Locate every Plasmodium ovale-infected red blood cell.
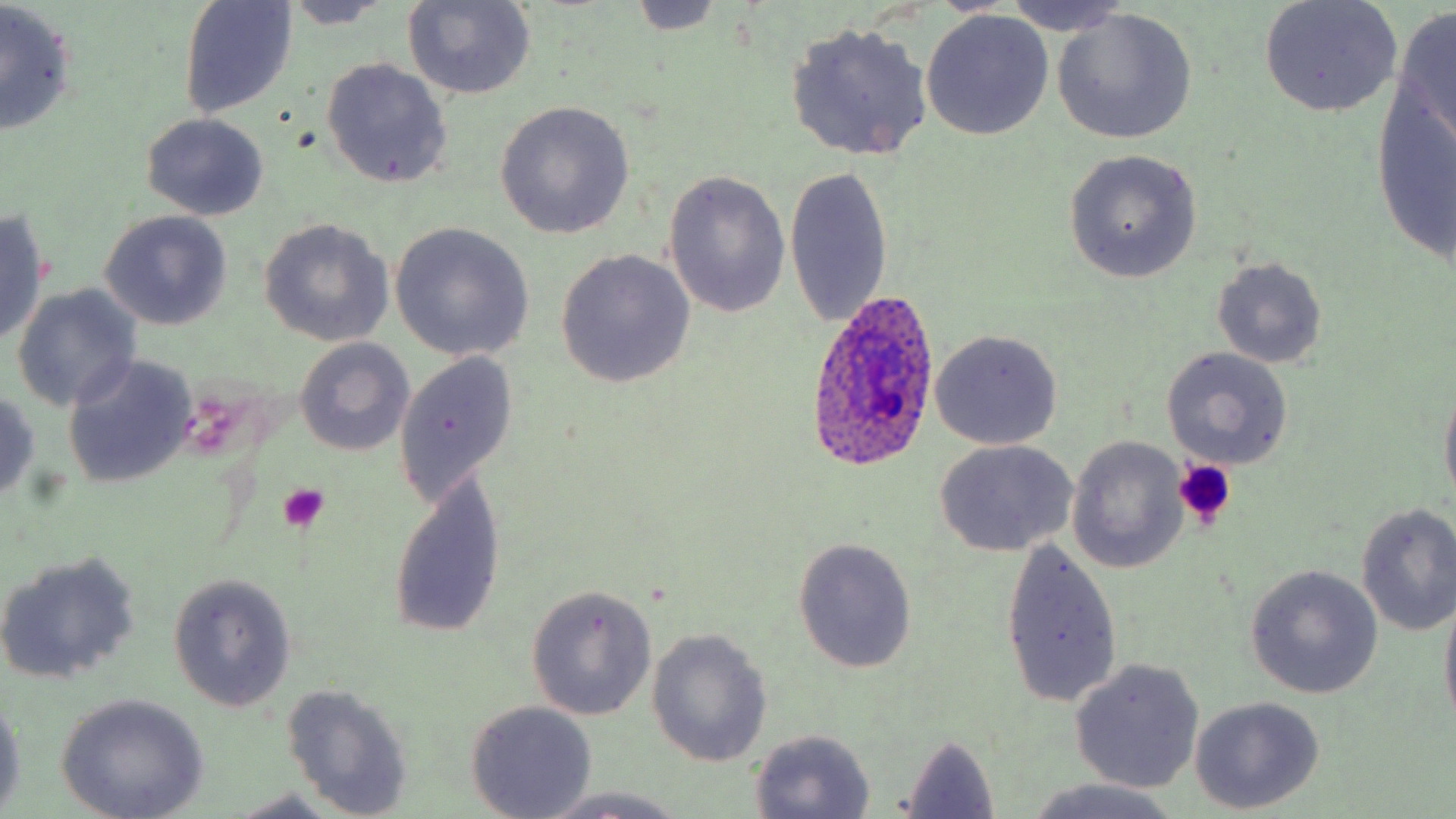
Approximate bounding boxes as named x1/y1/x2/y2 corners in pixels.
Plasmodium ovale-infected red blood cells: (x1=806, y1=290, x2=943, y2=469).

{
  "slide_level_diagnosis": "Plasmodium ovale",
  "stain": "May-Grünwald-Giemsa",
  "platelet_locations": "approximate bounding boxes as named x1/y1/x2/y2 corners in pixels: (x1=1173, y1=458, x2=1235, y2=531), (x1=278, y1=483, x2=329, y2=531)",
  "magnification": "1000x",
  "preparation": "thin blood film",
  "modality": "optical microscopy",
  "image_size": "1456×819 pixels",
  "uninfected_red_blood_cell_locations": "approximate bounding boxes as named x1/y1/x2/y2 corners in pixels: (x1=178, y1=0, x2=300, y2=120), (x1=1001, y1=0, x2=1135, y2=35), (x1=1258, y1=0, x2=1403, y2=118), (x1=278, y1=1, x2=396, y2=30), (x1=402, y1=1, x2=535, y2=101), (x1=0, y1=3, x2=77, y2=138), (x1=623, y1=4, x2=733, y2=35), (x1=1052, y1=8, x2=1197, y2=146), (x1=1391, y1=8, x2=1456, y2=150), (x1=921, y1=10, x2=1054, y2=140), (x1=785, y1=21, x2=934, y2=162), (x1=321, y1=58, x2=454, y2=188), (x1=1372, y1=79, x2=1456, y2=268), (x1=494, y1=101, x2=634, y2=238), (x1=141, y1=113, x2=270, y2=220), (x1=1065, y1=150, x2=1202, y2=282), (x1=782, y1=163, x2=894, y2=330), (x1=663, y1=169, x2=792, y2=320), (x1=0, y1=210, x2=51, y2=344), (x1=99, y1=210, x2=234, y2=330), (x1=259, y1=219, x2=394, y2=346), (x1=388, y1=222, x2=536, y2=362), (x1=47, y1=228, x2=203, y2=369), (x1=554, y1=250, x2=695, y2=388), (x1=1212, y1=258, x2=1326, y2=368), (x1=11, y1=284, x2=143, y2=412), (x1=930, y1=330, x2=1064, y2=450), (x1=293, y1=337, x2=415, y2=456), (x1=1161, y1=346, x2=1294, y2=470), (x1=394, y1=351, x2=518, y2=507), (x1=62, y1=354, x2=197, y2=490), (x1=1438, y1=382, x2=1456, y2=511), (x1=0, y1=388, x2=42, y2=502), (x1=1067, y1=436, x2=1189, y2=573), (x1=935, y1=440, x2=1077, y2=557), (x1=385, y1=469, x2=507, y2=641), (x1=1354, y1=501, x2=1456, y2=637), (x1=794, y1=536, x2=918, y2=673), (x1=998, y1=538, x2=1122, y2=711), (x1=0, y1=550, x2=142, y2=686), (x1=1246, y1=566, x2=1383, y2=699), (x1=166, y1=574, x2=298, y2=711), (x1=525, y1=585, x2=656, y2=720), (x1=1438, y1=588, x2=1456, y2=731), (x1=646, y1=629, x2=772, y2=766), (x1=1070, y1=659, x2=1204, y2=793), (x1=281, y1=682, x2=416, y2=817), (x1=0, y1=691, x2=25, y2=812), (x1=56, y1=694, x2=210, y2=819), (x1=1190, y1=697, x2=1324, y2=814), (x1=465, y1=700, x2=596, y2=817), (x1=747, y1=729, x2=877, y2=817), (x1=896, y1=734, x2=1001, y2=819), (x1=1019, y1=779, x2=1185, y2=819), (x1=531, y1=787, x2=697, y2=819), (x1=223, y1=791, x2=349, y2=818)",
  "field_of_view": "one of a larger specimen"
}